Classify this cell by malaria status.
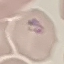

It is parasitized.

stain = Giemsa
capture = smartphone through the microscope eyepiece
preparation = thin blood smear
image type = cell patch, automatically extracted from a larger field of view and resized to 64 × 64 pixels